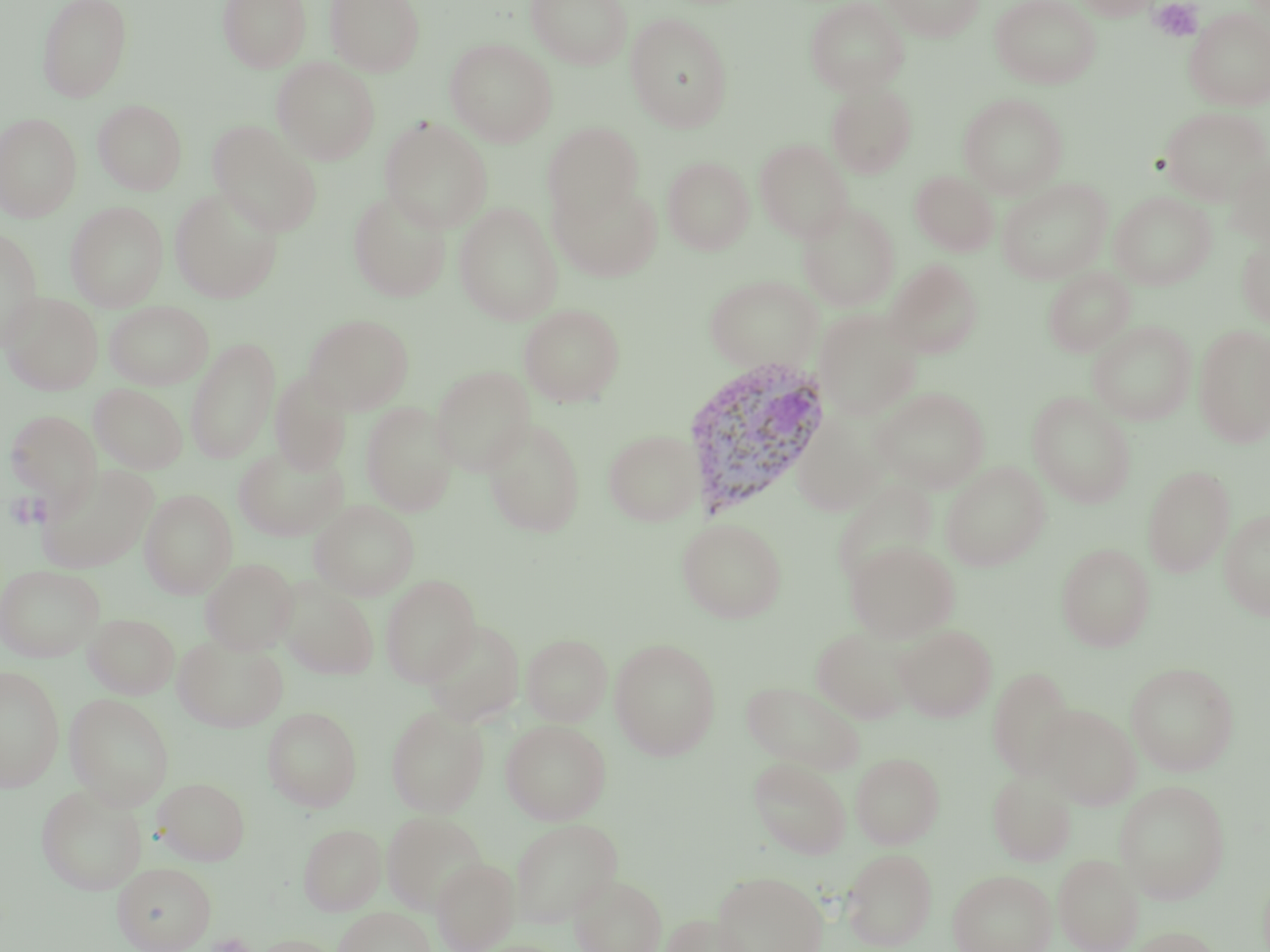

Summary:
  - Coordinate format: approximate bounding boxes as [x1, y1, x2, y2] in pixels
  - Plasmodium vivax-infected red blood cell locations: [680, 356, 834, 520]
  - Platelet locations: [1150, 1, 1203, 42], [5, 491, 46, 530], [207, 933, 255, 952]
  - Uninfected red blood cell locations: [37, 0, 133, 101], [218, 0, 311, 72], [327, 0, 425, 76], [526, 0, 633, 69], [805, 0, 909, 96], [882, 0, 983, 41], [990, 0, 1101, 89], [1075, 0, 1160, 20], [1185, 7, 1270, 111], [625, 14, 734, 132], [445, 38, 557, 146], [272, 57, 380, 164], [825, 81, 918, 178], [958, 93, 1068, 198], [93, 100, 187, 195], [1160, 106, 1269, 204], [0, 112, 82, 222], [379, 117, 493, 233], [208, 121, 323, 236], [543, 122, 643, 223], [754, 139, 853, 243], [1224, 152, 1270, 247], [663, 156, 754, 255], [910, 171, 998, 256], [997, 178, 1113, 284], [549, 180, 662, 281], [169, 187, 283, 303], [348, 190, 452, 302], [1110, 191, 1216, 289], [65, 201, 169, 311], [797, 201, 901, 311], [453, 202, 563, 325], [0, 226, 44, 349], [1237, 231, 1270, 328], [885, 259, 983, 358], [1043, 268, 1135, 356], [705, 275, 822, 372], [2, 292, 103, 395], [105, 301, 213, 390], [519, 304, 625, 407], [814, 310, 922, 419], [303, 314, 414, 414], [1088, 321, 1196, 425], [1194, 325, 1270, 447], [1061, 332, 1168, 459], [186, 336, 280, 464], [430, 366, 535, 474], [269, 371, 354, 474], [88, 384, 189, 474], [873, 387, 989, 492], [1027, 392, 1136, 507], [360, 402, 458, 517], [4, 409, 103, 515], [482, 416, 586, 537], [794, 416, 887, 516], [603, 427, 706, 526], [232, 444, 349, 542], [941, 461, 1050, 571], [37, 463, 158, 573], [1142, 465, 1235, 577], [832, 478, 938, 586], [139, 489, 238, 598], [309, 500, 419, 601], [1219, 509, 1270, 621], [677, 517, 787, 623], [845, 540, 959, 642], [1056, 543, 1155, 651], [200, 558, 298, 655], [0, 564, 105, 662], [381, 575, 481, 685], [276, 577, 380, 680], [83, 613, 180, 699], [421, 619, 526, 726], [894, 624, 997, 721], [811, 626, 916, 724], [172, 633, 290, 733], [522, 633, 612, 726], [609, 638, 720, 760], [1126, 661, 1239, 776], [0, 664, 65, 791], [988, 667, 1075, 780], [741, 679, 865, 774], [65, 694, 174, 810], [386, 704, 489, 816], [1039, 704, 1140, 809], [262, 706, 363, 811], [501, 719, 611, 824], [851, 751, 944, 849], [749, 757, 851, 859], [988, 769, 1077, 867], [154, 776, 249, 866], [1114, 780, 1230, 903], [36, 784, 147, 895], [382, 811, 487, 914], [509, 818, 622, 927], [298, 823, 386, 915], [841, 847, 937, 950], [1053, 854, 1144, 952], [431, 858, 520, 951], [112, 861, 216, 952], [948, 869, 1056, 952], [711, 870, 827, 952], [569, 873, 667, 952], [334, 906, 435, 952], [658, 913, 755, 952], [1125, 926, 1223, 952], [248, 935, 345, 952]
  - Slide-level diagnosis: Plasmodium vivax
  - Magnification: 1000x
  - Modality: light microscopy
  - Stain: May-Grünwald-Giemsa
  - Image size: 1270×952 pixels
  - Field of view: single
  - Preparation: thin blood film